Point out each Plasmodium parasite.
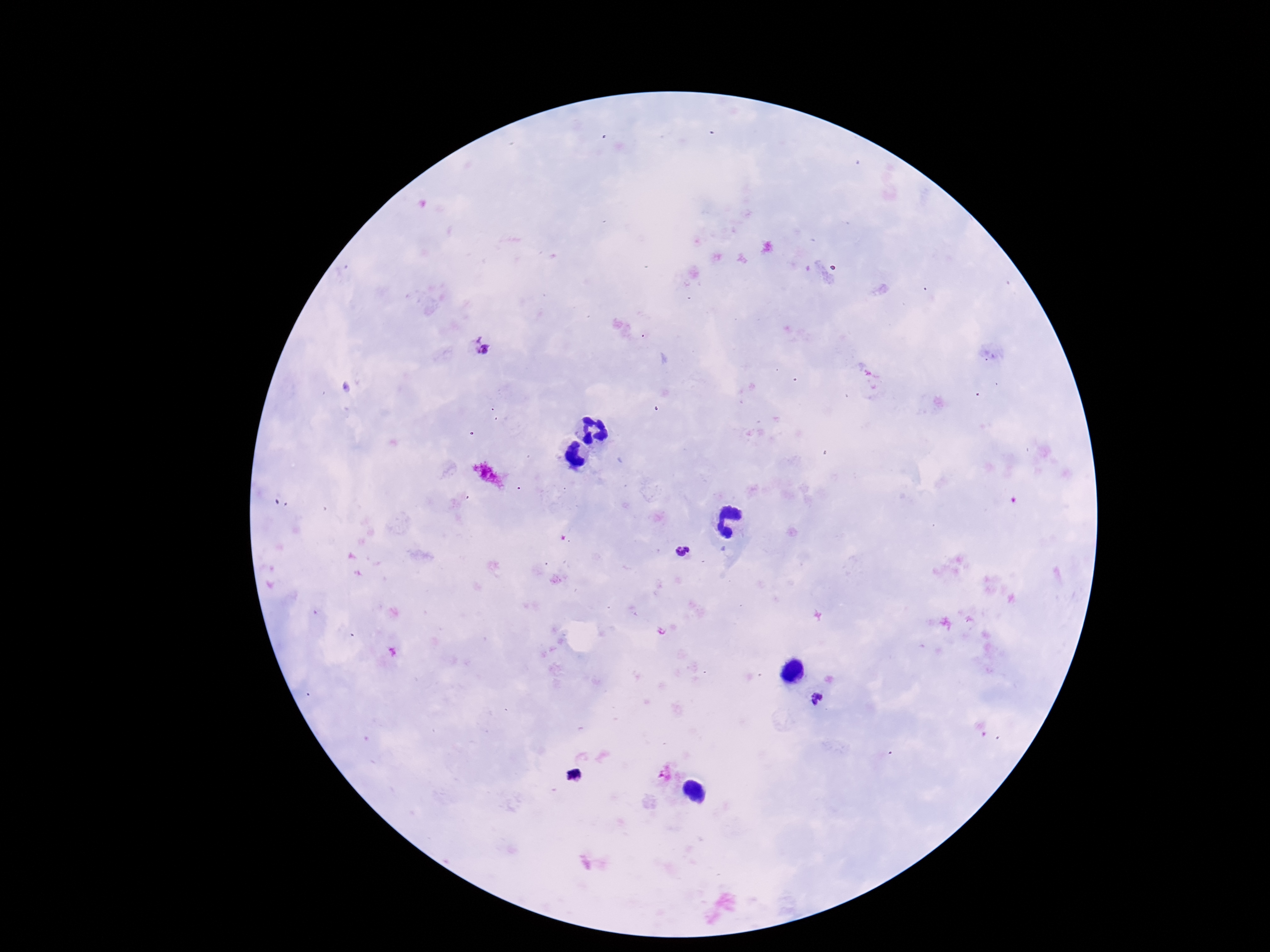

Approximate object centers, in pixels from the top-left corner.
Plasmodium parasites: (x=483, y=348), (x=683, y=553), (x=818, y=700).

capture = smartphone camera through the microscope eyepiece
magnification = 100x
image size = 1270×952 pixels
stain = Giemsa
preparation = thick blood film
field of view = single
patient malaria status = positive